Evaluate for Plasmodium parasites.
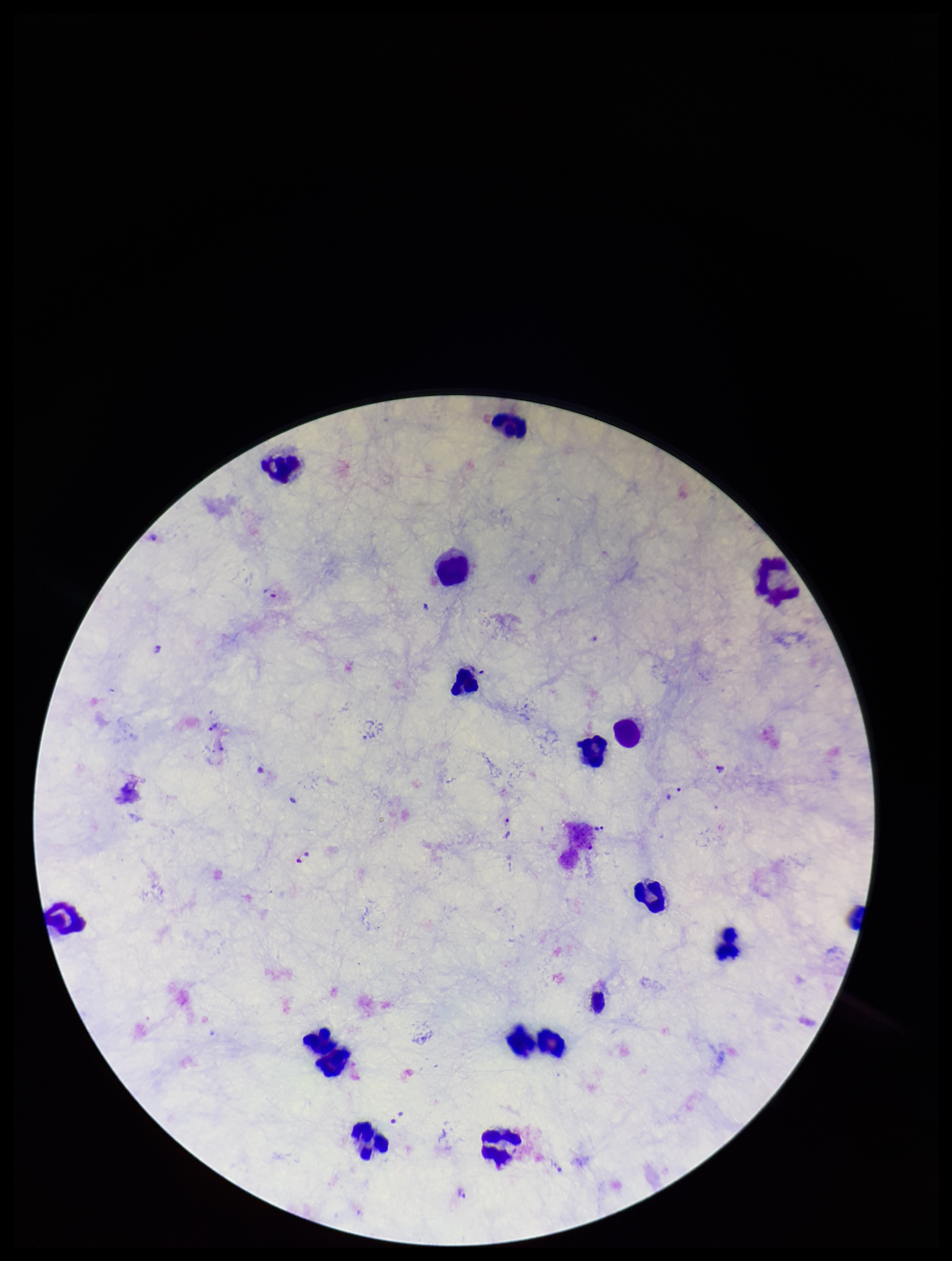
Detected.

field of view = one from this slide
capture = smartphone photograph through the microscope eyepiece
preparation = thick smear
parasite count = 8
species reported for this patient = Plasmodium vivax
image size = 952×1261 pixels
leukocyte count = 15
stain = Giemsa
patient malaria status = infected